Outline each Plasmodium falciparum-infected red blood cell.
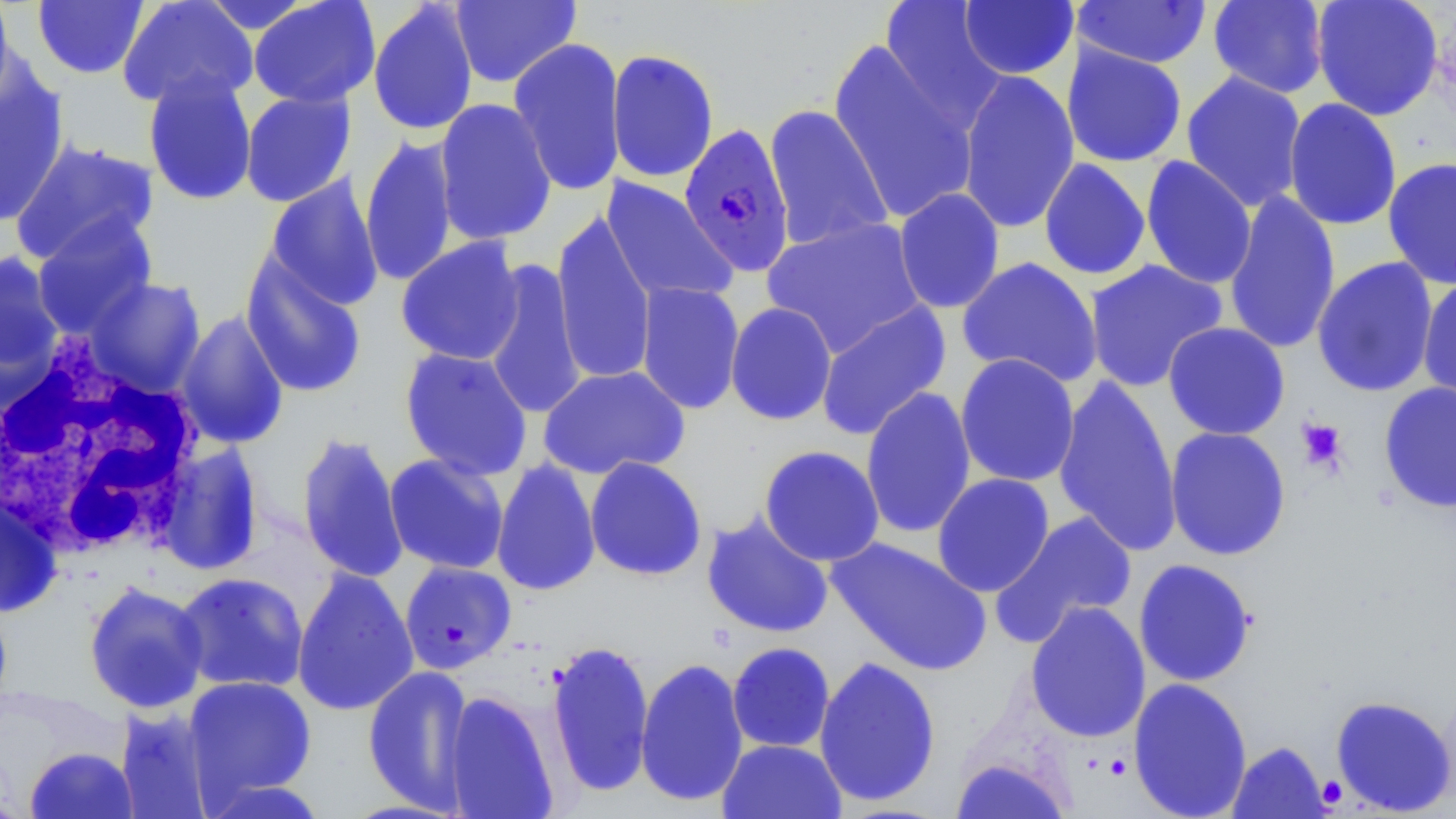
Approximate bounding boxes as (x1, y1, x2, y2) in pixels.
Plasmodium falciparum-infected red blood cells: (679, 122, 795, 277).

Platelet locations: (1296, 417, 1348, 473). Uninfected red blood cell locations: (0, 0, 16, 107), (32, 0, 149, 79), (117, 0, 258, 110), (248, 0, 381, 109), (450, 0, 580, 88), (880, 0, 1006, 127), (958, 0, 1079, 80), (1073, 0, 1212, 69), (1208, 0, 1329, 99), (1311, 0, 1444, 121), (198, 1, 316, 35), (367, 1, 479, 137), (508, 37, 626, 197), (828, 38, 980, 226), (1062, 43, 1187, 168), (606, 49, 719, 183), (0, 70, 69, 227), (958, 70, 1080, 234), (142, 71, 257, 206), (1181, 71, 1308, 212), (240, 90, 355, 207), (434, 98, 557, 246), (1283, 98, 1402, 231), (764, 104, 893, 253), (360, 133, 459, 288), (10, 139, 160, 267), (1140, 156, 1257, 290), (1383, 157, 1456, 290), (1039, 158, 1151, 280), (262, 175, 384, 311), (601, 177, 739, 306), (893, 188, 1005, 314), (1223, 190, 1341, 355), (551, 211, 657, 385), (31, 215, 157, 338), (761, 217, 927, 357), (396, 236, 525, 366), (0, 250, 65, 393), (240, 255, 368, 399), (957, 257, 1103, 389), (1312, 257, 1439, 397), (482, 259, 586, 421), (1084, 259, 1228, 393), (84, 277, 206, 398), (1417, 277, 1456, 406), (634, 282, 745, 415), (815, 301, 951, 441), (725, 302, 837, 426), (175, 309, 289, 449), (1163, 321, 1290, 440), (399, 347, 533, 482), (955, 354, 1080, 487), (538, 365, 690, 480), (1053, 375, 1182, 555), (1379, 382, 1456, 513), (860, 386, 977, 539), (1164, 426, 1291, 561), (296, 431, 408, 584), (153, 442, 265, 575), (759, 445, 884, 566), (384, 453, 509, 575), (585, 456, 707, 581), (491, 458, 601, 596), (932, 473, 1055, 597), (0, 491, 63, 618), (994, 510, 1139, 644), (701, 511, 834, 639), (826, 537, 992, 676), (1133, 558, 1257, 687), (399, 561, 517, 673), (291, 567, 419, 717), (174, 571, 309, 693), (83, 581, 209, 715), (1025, 600, 1151, 742), (545, 639, 655, 799), (727, 642, 835, 752), (813, 655, 941, 807), (635, 656, 749, 808), (362, 664, 475, 814), (182, 675, 317, 806), (1128, 677, 1253, 819), (443, 691, 559, 818), (1331, 695, 1455, 815), (114, 706, 215, 819), (717, 739, 846, 819), (1227, 741, 1330, 818), (24, 747, 138, 819), (950, 756, 1073, 819), (199, 775, 333, 819). White blood cell locations: (0, 341, 207, 560). Slide-level diagnosis: Plasmodium falciparum. Light microscopy. May-Grünwald-Giemsa-stained preparation. One field of a larger specimen. 1000x magnification. Thin blood film. Image is 1456×819 pixels.